Identify the cell.
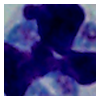

A leukocyte.

modality = photomicrograph
magnification = 1000x